Give the extent of all Plasmodium malariae-infected red blood cells.
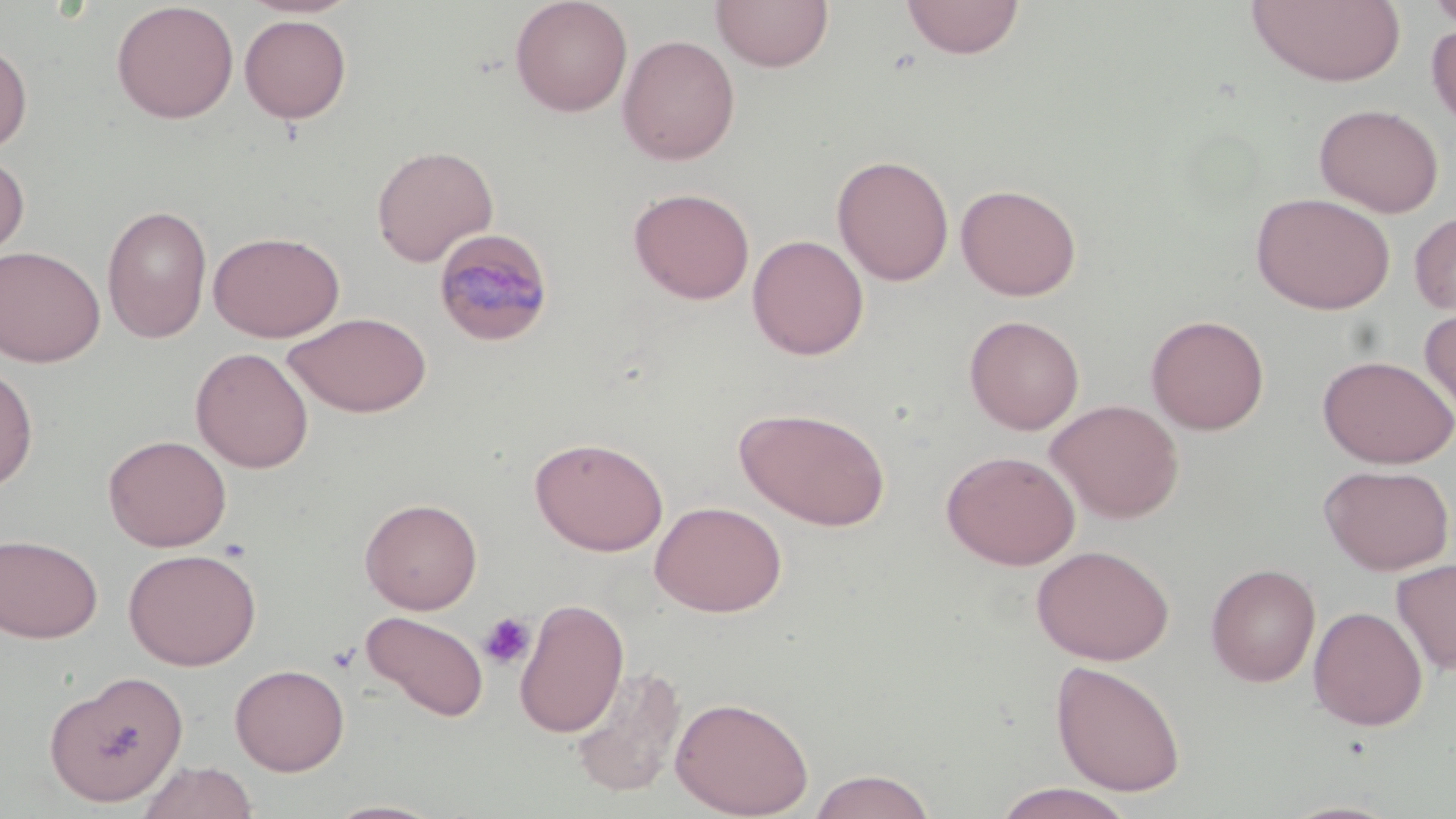

Approximate bounding boxes as [x1, y1, x2, y2] in pixels.
Plasmodium malariae-infected red blood cells: [432, 228, 555, 348].

Summary:
  - Uninfected red blood cell locations: [236, 0, 362, 19], [509, 0, 633, 117], [711, 0, 834, 73], [901, 0, 1025, 60], [1246, 0, 1406, 87], [1427, 0, 1456, 31], [111, 1, 239, 124], [239, 14, 352, 124], [1427, 22, 1456, 132], [617, 34, 740, 165], [0, 41, 33, 155], [1313, 103, 1445, 218], [371, 145, 498, 267], [0, 153, 30, 265], [831, 154, 955, 286], [956, 183, 1082, 301], [628, 187, 755, 305], [1251, 192, 1396, 314], [101, 205, 213, 343], [1409, 210, 1456, 317], [208, 231, 344, 342], [747, 234, 869, 360], [0, 245, 105, 367], [1419, 303, 1456, 423], [284, 311, 432, 418], [1146, 314, 1270, 435], [964, 315, 1085, 435], [191, 347, 314, 473], [1317, 354, 1456, 469], [0, 365, 38, 493], [1046, 398, 1184, 523], [735, 406, 891, 531], [102, 434, 232, 552], [530, 437, 668, 556], [941, 449, 1081, 570], [1319, 463, 1454, 575], [360, 497, 482, 614], [650, 500, 787, 617], [0, 534, 103, 643], [1031, 544, 1175, 666], [123, 548, 262, 670], [1392, 558, 1456, 675], [1205, 563, 1321, 687], [514, 596, 629, 738], [1308, 606, 1428, 730], [360, 611, 489, 722], [1050, 659, 1187, 797], [230, 663, 349, 775], [570, 665, 686, 797], [44, 670, 188, 807], [671, 696, 814, 818], [136, 760, 258, 819], [806, 769, 938, 818], [990, 783, 1137, 819], [324, 799, 447, 818]
  - Platelet locations: [479, 612, 536, 670]
  - Slide-level diagnosis: Plasmodium malariae
  - Magnification: 1000x
  - Preparation: thin blood smear
  - Modality: light microscopy
  - Stain: May-Grünwald-Giemsa
  - Field of view: single
  - Image size: 1456×819 pixels